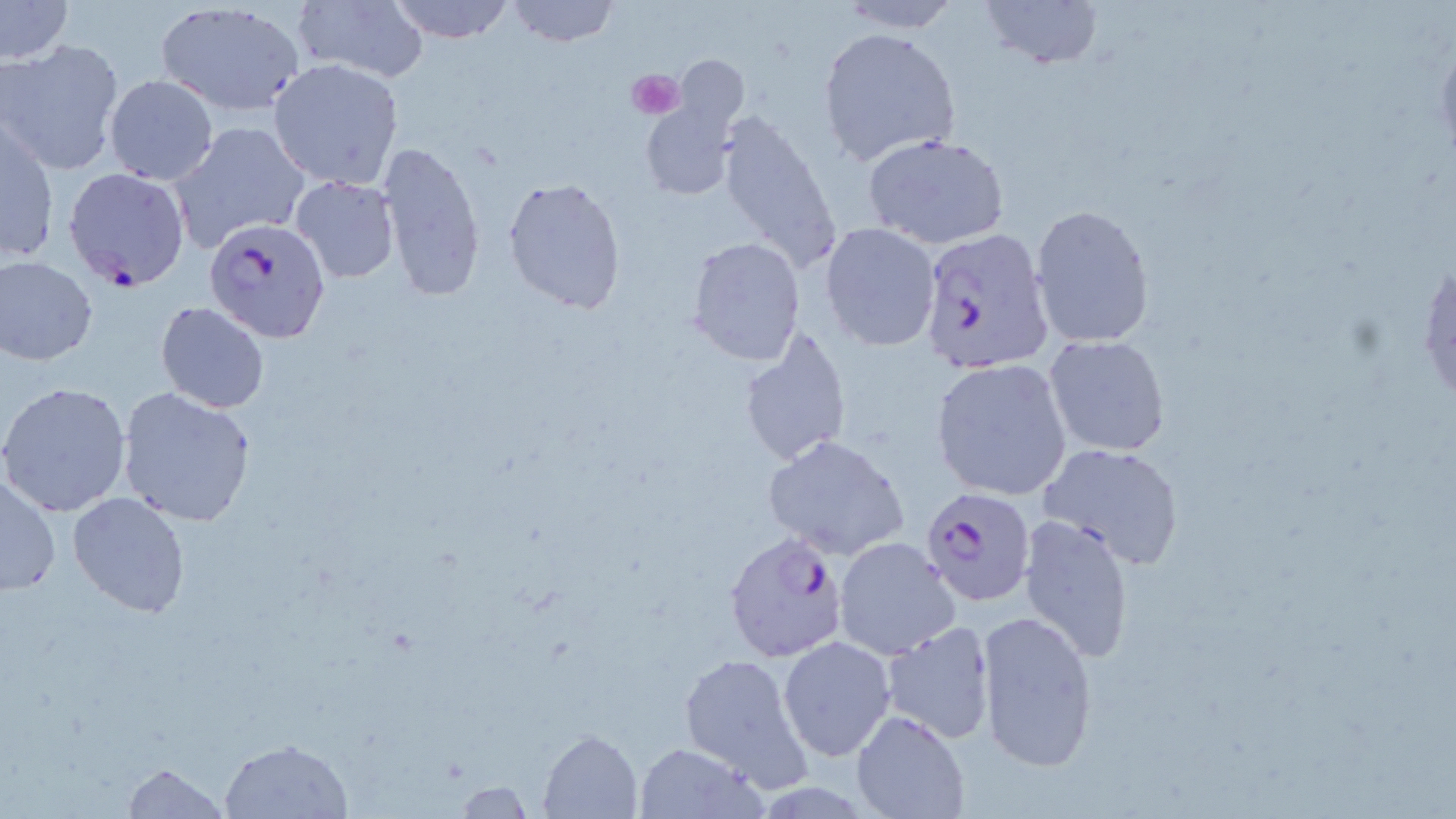
slide-level diagnosis = Plasmodium falciparum
image size = 1456×819 pixels
modality = light microscopy
field of view = one of a larger specimen
platelet locations = approximate bounding boxes as (x1,y1)-(x2,y2) corner pairs in pixels: (626,69)-(686,119)
magnification = 1000x
preparation = thin blood smear
Plasmodium falciparum-infected red blood cell locations = approximate bounding boxes as (x1,y1)-(x2,y2) corner pairs in pixels: (63,166)-(191,290), (204,216)-(331,342), (917,226)-(1052,375), (920,486)-(1036,607), (722,530)-(852,661)
stain = May-Grünwald-Giemsa
uninfected red blood cell locations = approximate bounding boxes as (x1,y1)-(x2,y2) corner pairs in pixels: (292,0)-(430,85), (386,0)-(515,43), (505,0)-(618,46), (977,0)-(1106,73), (1,1)-(74,64), (154,1)-(306,117), (833,1)-(965,33), (818,25)-(960,168), (0,38)-(126,176), (674,56)-(748,132), (268,58)-(404,191), (103,75)-(218,186), (639,103)-(736,202), (712,111)-(840,273), (1,118)-(58,266), (170,121)-(310,251), (863,132)-(1011,249), (373,140)-(486,300), (290,175)-(400,283), (503,178)-(626,314), (1029,202)-(1155,348), (821,223)-(941,351), (686,238)-(806,366), (1416,249)-(1455,419), (0,253)-(98,366), (155,302)-(271,415), (736,328)-(852,467), (1043,336)-(1170,457), (931,361)-(1072,499), (0,382)-(132,518), (115,384)-(260,526), (762,434)-(911,560), (1040,443)-(1185,569), (1,474)-(62,597), (67,493)-(191,617), (1018,513)-(1136,663), (834,537)-(959,658), (975,609)-(1101,777), (878,622)-(998,743), (779,637)-(897,760), (678,652)-(815,793), (853,710)-(969,818), (538,729)-(643,818), (219,737)-(354,818), (632,741)-(767,817), (120,760)-(230,818), (455,779)-(533,817)